Identify the parasite.
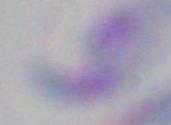

Toxoplasma gondii.

modality = micrograph
magnification = 1000x